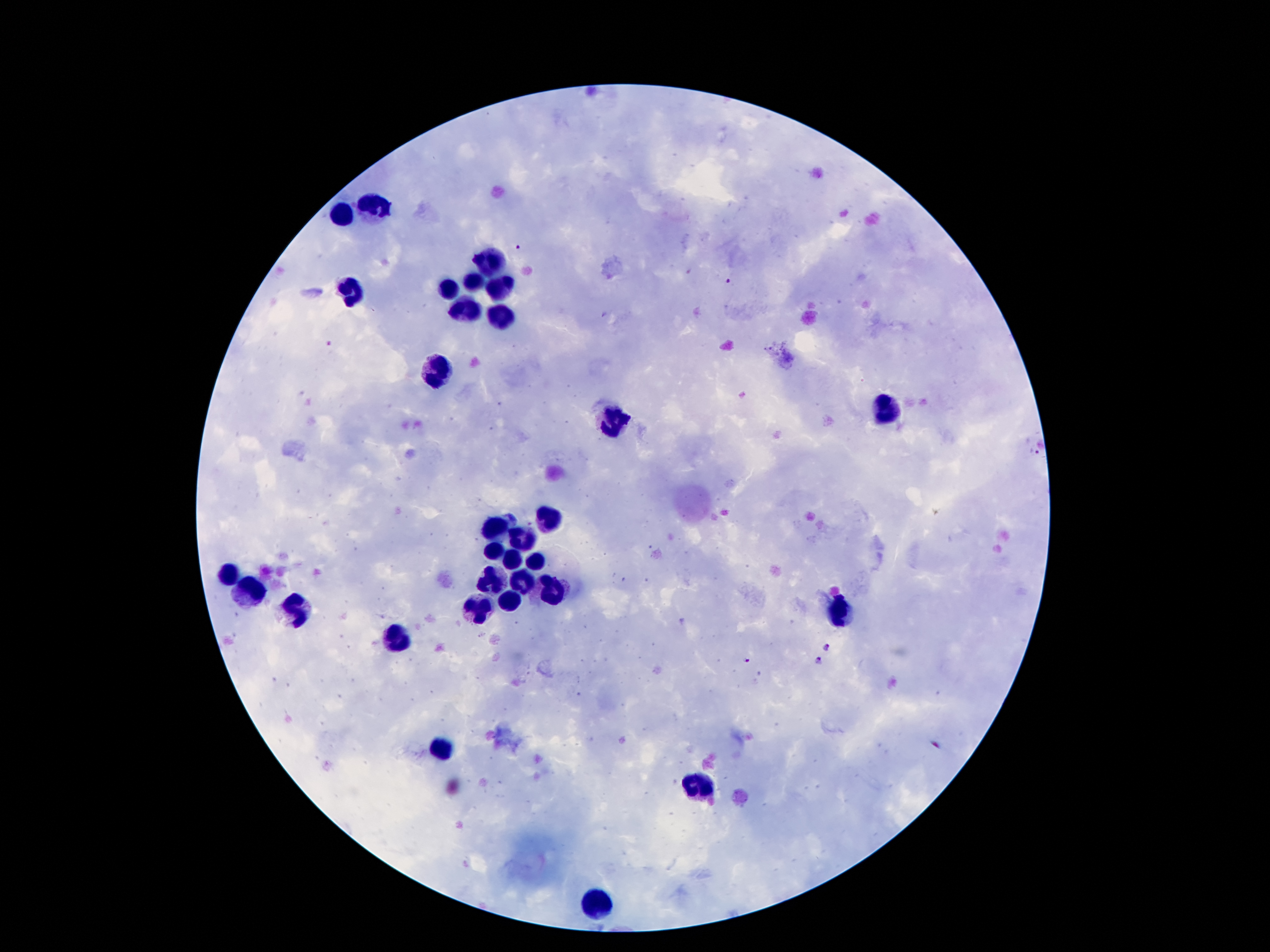

Approximate centers as (x, y) in pixels. Malaria parasite locations: (517, 246), (730, 283), (330, 345), (1033, 452), (828, 648), (746, 660), (818, 662), (935, 744). Leukocyte locations: (377, 205), (342, 215), (490, 260), (472, 280), (503, 286), (448, 289), (352, 291), (466, 312), (506, 320), (435, 370), (882, 413), (614, 422), (550, 516), (498, 526), (522, 536), (494, 549), (509, 560), (532, 561), (227, 574), (494, 577), (524, 580), (250, 592), (552, 592), (509, 600), (476, 609), (298, 610), (837, 613), (395, 635), (445, 745), (698, 783), (596, 902). Single field of view. Smartphone photograph taken through the microscope eyepiece. Patient malaria status: infected with Plasmodium falciparum. Thick blood film. 100x magnification. Image is 1270×952 pixels. Giemsa stain.